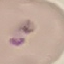
result: no malaria parasites seen
stain: Giemsa
capture: smartphone through the microscope eyepiece
preparation: thin blood smear
image_type: automatically extracted cell patch, resized to 64 × 64 pixels